Identify the preparation type.
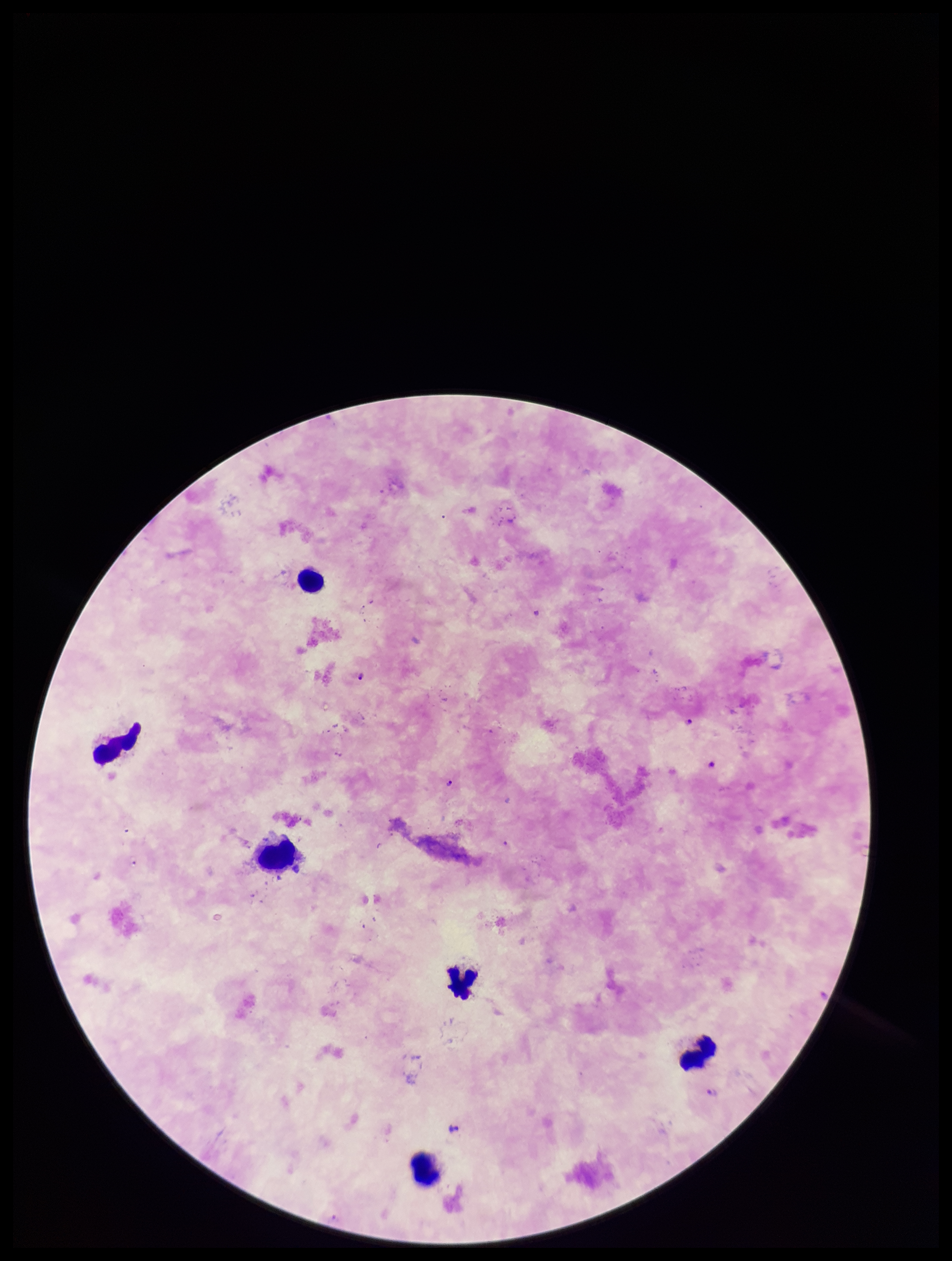
A thick smear.

Plasmodium parasites: seen. Giemsa stain. Patient malaria status: positive. Parasite count: 5. One field from this slide. Leukocyte count: 6. Species reported for this patient: Plasmodium falciparum. Smartphone photograph taken through the eyepiece of a microscope. Image is 952×1261 pixels.